Give the extent of all Plasmodium falciparum-infected red blood cells.
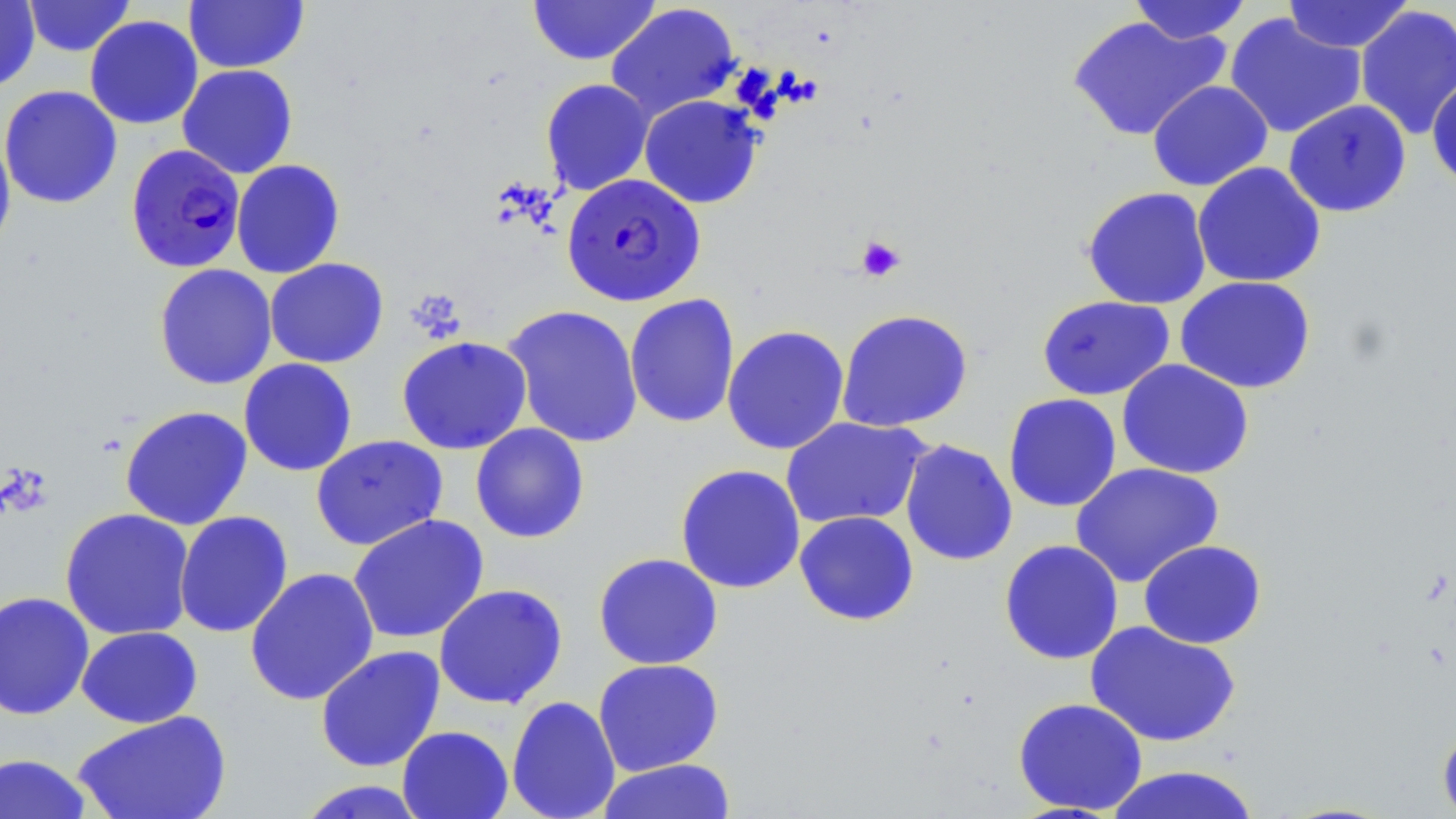
Approximate bounding boxes as (x1, y1, x2, y2) in pixels.
Plasmodium falciparum-infected red blood cells: (126, 143, 246, 273), (561, 173, 705, 307).

Uninfected red blood cell locations: (23, 0, 136, 57), (183, 0, 309, 74), (528, 0, 661, 65), (1128, 0, 1252, 44), (1281, 0, 1413, 53), (0, 1, 40, 91), (605, 4, 740, 120), (1354, 4, 1456, 141), (1224, 13, 1366, 139), (84, 15, 204, 130), (1067, 15, 1229, 141), (177, 64, 298, 179), (1427, 75, 1456, 191), (540, 78, 655, 195), (1147, 80, 1273, 191), (0, 85, 123, 209), (638, 94, 763, 209), (1283, 99, 1412, 217), (0, 125, 16, 258), (231, 159, 345, 279), (1192, 162, 1326, 288), (1081, 186, 1212, 310), (264, 258, 389, 368), (154, 264, 278, 390), (1174, 275, 1316, 394), (624, 293, 740, 429), (1037, 295, 1175, 401), (502, 304, 644, 448), (835, 309, 974, 433), (722, 324, 850, 455), (396, 335, 533, 455), (238, 358, 358, 477), (1117, 359, 1255, 479), (1002, 393, 1122, 513), (120, 405, 253, 530), (781, 416, 930, 529), (470, 423, 590, 544), (310, 435, 448, 551), (899, 438, 1018, 566), (1070, 462, 1224, 588), (675, 464, 806, 594), (59, 508, 195, 641), (174, 511, 293, 638), (794, 511, 919, 627), (347, 514, 489, 644), (999, 539, 1124, 665), (1138, 539, 1267, 649), (593, 553, 723, 670), (244, 567, 380, 707), (433, 583, 568, 709), (0, 590, 95, 721), (1084, 621, 1241, 748), (76, 626, 203, 728), (315, 645, 446, 773), (592, 658, 724, 776), (506, 695, 620, 819), (1013, 697, 1148, 815), (71, 710, 232, 819), (1437, 723, 1456, 819), (397, 725, 514, 819), (0, 753, 96, 818), (596, 758, 738, 819), (1104, 765, 1262, 819), (293, 780, 433, 818). Platelet locations: (856, 236, 906, 281). Slide-level diagnosis: Plasmodium falciparum. One field of a larger specimen. 1000x magnification. Image is 1456×819 pixels. May-Grünwald-Giemsa-stained preparation. Light microscopy. Thin blood smear.